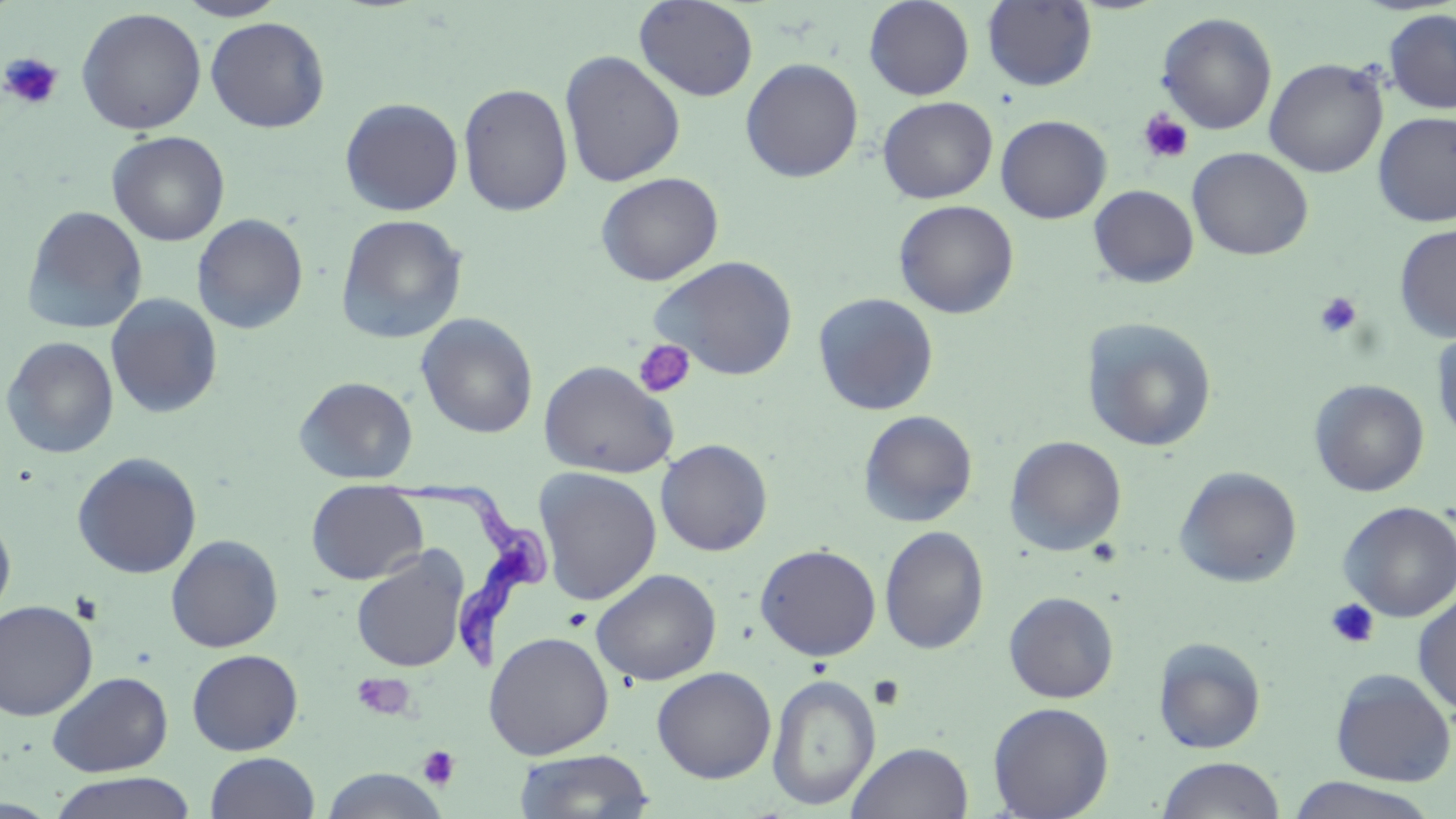 Approximate bounding boxes as (x1,y1)-(x2,y2) corner pairs in pixels. Trypanosoma brucei locations: (374,476)-(555,671). Uninfected red blood cell locations: (173,0)-(289,21), (634,0)-(759,102), (864,0)-(974,100), (982,1)-(1098,91), (76,7)-(207,135), (1384,9)-(1456,114), (1156,12)-(1277,134), (205,16)-(330,133), (559,50)-(686,187), (740,58)-(864,183), (1264,58)-(1388,178), (458,82)-(573,217), (878,96)-(998,203), (339,97)-(463,216), (1372,111)-(1456,227), (995,114)-(1112,223), (107,131)-(230,246), (1187,147)-(1314,261), (596,172)-(723,286), (1088,185)-(1199,288), (893,199)-(1019,319), (21,205)-(148,334), (191,214)-(309,335), (334,214)-(468,345), (1394,224)-(1456,342), (649,254)-(799,381), (813,292)-(939,415), (105,293)-(223,419), (416,312)-(539,439), (1080,317)-(1218,452), (1431,325)-(1456,448), (2,336)-(119,459), (538,360)-(677,479), (294,376)-(418,484), (1309,380)-(1429,497), (859,410)-(978,528), (1005,436)-(1127,557), (655,439)-(773,556), (72,452)-(202,579), (1174,466)-(1302,588), (534,467)-(662,605), (306,481)-(428,585), (1338,500)-(1456,622), (0,514)-(16,623), (879,525)-(989,655), (165,534)-(284,653), (754,544)-(881,661), (351,549)-(469,673), (591,568)-(721,687), (1003,591)-(1119,703), (1413,593)-(1456,716), (0,600)-(98,720), (484,631)-(614,759), (1153,637)-(1267,754), (186,649)-(303,755), (651,666)-(776,783), (1330,669)-(1455,786), (47,670)-(173,777), (767,673)-(881,810), (988,702)-(1114,818), (847,741)-(974,819), (513,748)-(655,819), (205,752)-(320,819), (1156,756)-(1286,819), (319,768)-(449,818), (47,771)-(199,819), (1281,776)-(1443,819). Platelet locations: (0,52)-(64,110), (1138,109)-(1194,165), (1314,292)-(1363,337), (633,339)-(696,398), (1325,598)-(1380,650), (562,608)-(592,632), (353,674)-(414,721), (869,676)-(906,710), (417,746)-(460,791). Slide-level diagnosis: Trypanosoma brucei. Image is 1456×819 pixels. May-Grünwald-Giemsa stain. 1000x magnification. Single field of view. Optical microscopy. Thin blood film.